Locate platelets.
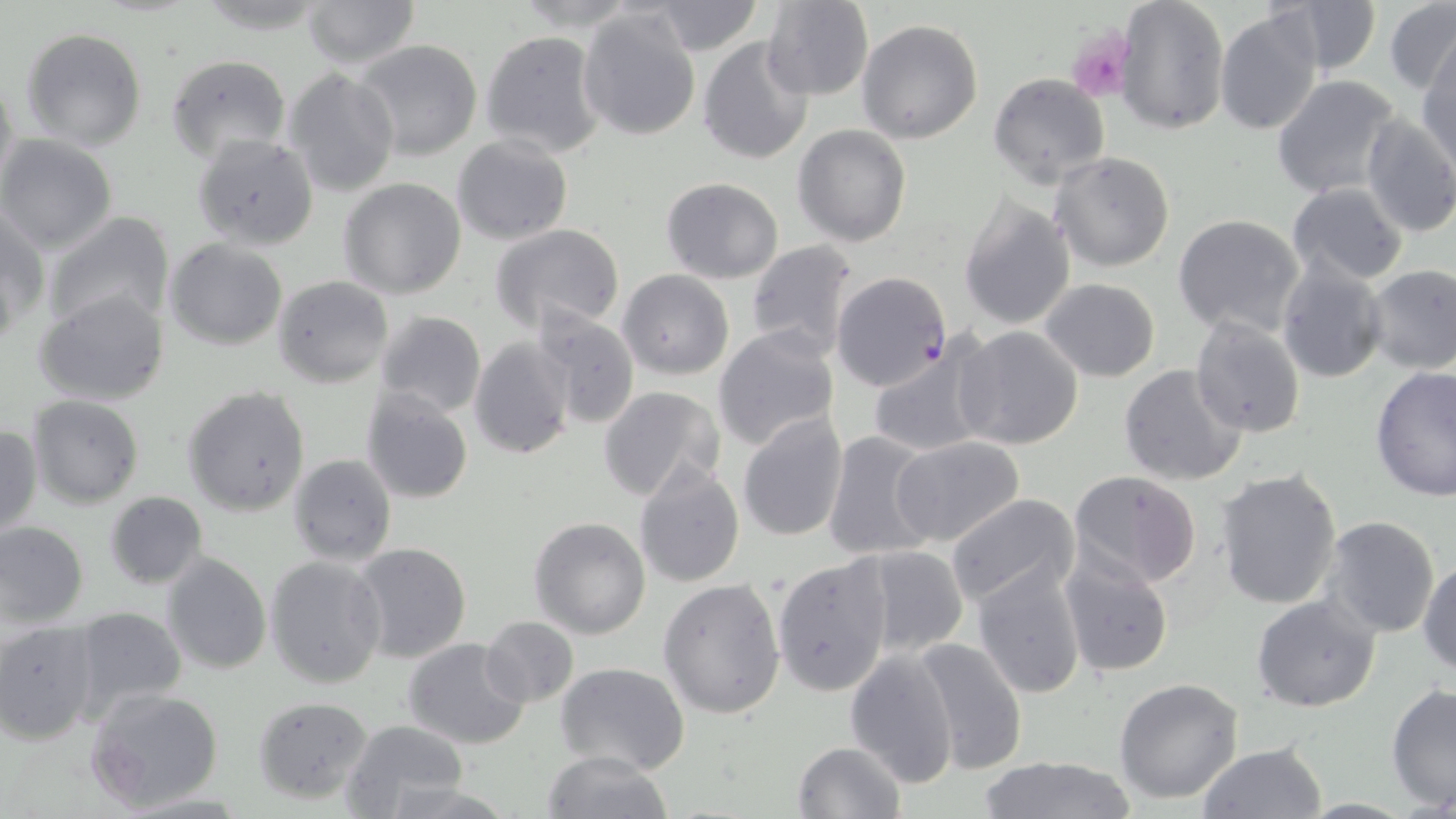
Approximate bounding boxes as named x1/y1/x2/y2 corners in pixels.
Platelets: (x1=1067, y1=25, x2=1132, y2=101).

Plasmodium falciparum-infected red blood cell locations: (x1=831, y1=271, x2=952, y2=393). Uninfected red blood cell locations: (x1=299, y1=0, x2=422, y2=69), (x1=760, y1=0, x2=873, y2=101), (x1=1116, y1=0, x2=1231, y2=137), (x1=1273, y1=0, x2=1381, y2=76), (x1=646, y1=1, x2=766, y2=55), (x1=1383, y1=1, x2=1456, y2=94), (x1=578, y1=5, x2=704, y2=142), (x1=1214, y1=7, x2=1325, y2=137), (x1=856, y1=19, x2=984, y2=144), (x1=20, y1=26, x2=148, y2=151), (x1=480, y1=29, x2=606, y2=158), (x1=699, y1=36, x2=816, y2=164), (x1=355, y1=39, x2=482, y2=162), (x1=1419, y1=43, x2=1456, y2=169), (x1=165, y1=53, x2=292, y2=165), (x1=1, y1=68, x2=20, y2=200), (x1=283, y1=68, x2=400, y2=197), (x1=988, y1=73, x2=1110, y2=188), (x1=1271, y1=76, x2=1402, y2=201), (x1=1357, y1=113, x2=1456, y2=238), (x1=793, y1=124, x2=912, y2=246), (x1=0, y1=134, x2=119, y2=255), (x1=451, y1=134, x2=572, y2=245), (x1=1049, y1=152, x2=1177, y2=273), (x1=338, y1=178, x2=467, y2=300), (x1=661, y1=178, x2=784, y2=283), (x1=1285, y1=183, x2=1411, y2=286), (x1=957, y1=194, x2=1076, y2=333), (x1=1, y1=206, x2=46, y2=342), (x1=43, y1=212, x2=175, y2=335), (x1=1171, y1=214, x2=1307, y2=339), (x1=491, y1=224, x2=627, y2=332), (x1=165, y1=237, x2=288, y2=350), (x1=743, y1=239, x2=857, y2=360), (x1=1275, y1=258, x2=1389, y2=384), (x1=1363, y1=265, x2=1456, y2=374), (x1=618, y1=269, x2=735, y2=379), (x1=272, y1=275, x2=395, y2=387), (x1=1040, y1=278, x2=1161, y2=381), (x1=35, y1=289, x2=171, y2=406), (x1=530, y1=306, x2=640, y2=430), (x1=375, y1=310, x2=486, y2=419), (x1=1189, y1=314, x2=1308, y2=440), (x1=712, y1=325, x2=841, y2=452), (x1=953, y1=325, x2=1086, y2=451), (x1=469, y1=336, x2=575, y2=460), (x1=866, y1=339, x2=994, y2=459), (x1=1119, y1=362, x2=1249, y2=487), (x1=1370, y1=365, x2=1456, y2=501), (x1=181, y1=385, x2=313, y2=518), (x1=596, y1=385, x2=726, y2=502), (x1=359, y1=386, x2=474, y2=504), (x1=27, y1=395, x2=145, y2=509), (x1=736, y1=413, x2=848, y2=541), (x1=0, y1=423, x2=41, y2=541), (x1=822, y1=431, x2=939, y2=562), (x1=891, y1=436, x2=1025, y2=548), (x1=288, y1=453, x2=396, y2=567), (x1=631, y1=462, x2=745, y2=589), (x1=1214, y1=468, x2=1344, y2=609), (x1=1068, y1=472, x2=1204, y2=589), (x1=104, y1=491, x2=208, y2=588), (x1=943, y1=493, x2=1081, y2=611), (x1=1319, y1=516, x2=1441, y2=638), (x1=530, y1=517, x2=651, y2=639), (x1=0, y1=521, x2=89, y2=626), (x1=352, y1=542, x2=471, y2=663), (x1=852, y1=544, x2=971, y2=657), (x1=1058, y1=550, x2=1175, y2=677), (x1=161, y1=553, x2=272, y2=675), (x1=772, y1=554, x2=893, y2=696), (x1=264, y1=555, x2=388, y2=690), (x1=1418, y1=557, x2=1456, y2=676), (x1=972, y1=560, x2=1088, y2=701), (x1=658, y1=577, x2=787, y2=719), (x1=1250, y1=594, x2=1381, y2=713), (x1=67, y1=606, x2=189, y2=723), (x1=479, y1=617, x2=579, y2=708), (x1=0, y1=620, x2=100, y2=745), (x1=911, y1=637, x2=1028, y2=770), (x1=403, y1=638, x2=530, y2=750), (x1=844, y1=648, x2=961, y2=790), (x1=555, y1=662, x2=690, y2=776), (x1=1114, y1=677, x2=1244, y2=805), (x1=1386, y1=682, x2=1456, y2=813), (x1=85, y1=687, x2=224, y2=812), (x1=252, y1=696, x2=375, y2=805), (x1=339, y1=718, x2=469, y2=818), (x1=791, y1=741, x2=906, y2=819), (x1=1195, y1=743, x2=1328, y2=819), (x1=539, y1=751, x2=675, y2=819), (x1=975, y1=755, x2=1137, y2=819). Slide-level diagnosis: Plasmodium falciparum. One field of a larger specimen. Captured at 1000x magnification. May-Grünwald-Giemsa stain. Light microscopy. Thin blood smear. Image is 1456×819 pixels.